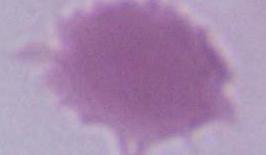
1000x magnification. Micrograph. A red blood cell is shown.